Give the position of every Plasmodium parasite.
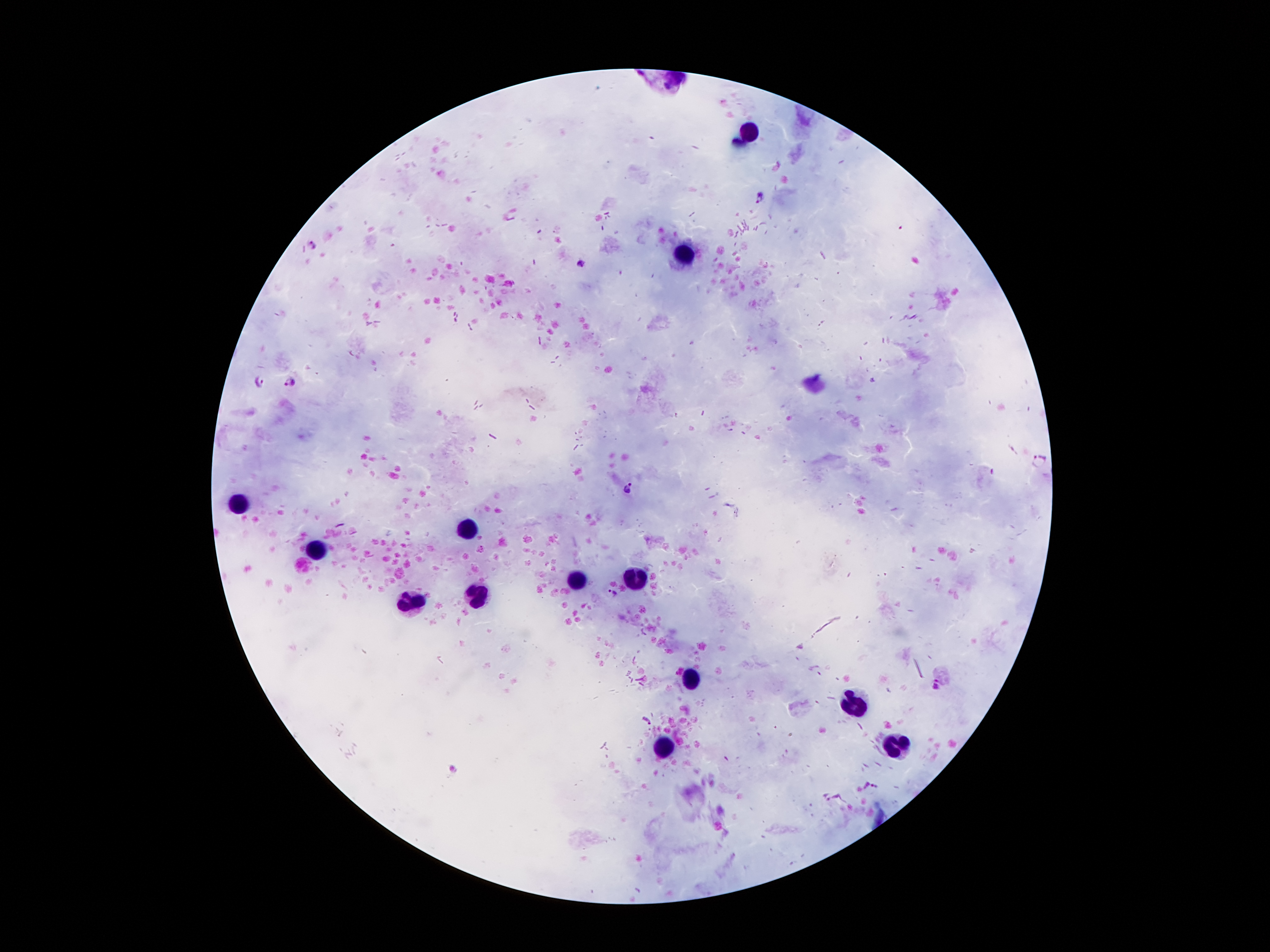
Approximate centers as {x, y} in pixels.
Plasmodium parasites: {760, 197}, {582, 263}, {260, 381}, {290, 381}, {627, 485}, {612, 594}, {937, 685}, {647, 721}, {875, 786}, {825, 797}.

{
  "image_size": "1270×952 pixels",
  "patient_malaria_status": "positive for Plasmodium falciparum",
  "stain": "Giemsa",
  "field_of_view": "one from this slide",
  "leukocyte_locations": "approximate centers as {x, y} in pixels: {748, 135}, {689, 259}, {233, 505}, {468, 530}, {314, 552}, {637, 578}, {575, 581}, {479, 596}, {409, 605}, {692, 677}, {851, 702}, {899, 746}, {662, 748}",
  "capture": "smartphone through the microscope eyepiece",
  "preparation": "thick peripheral-blood smear",
  "magnification": "100x"
}